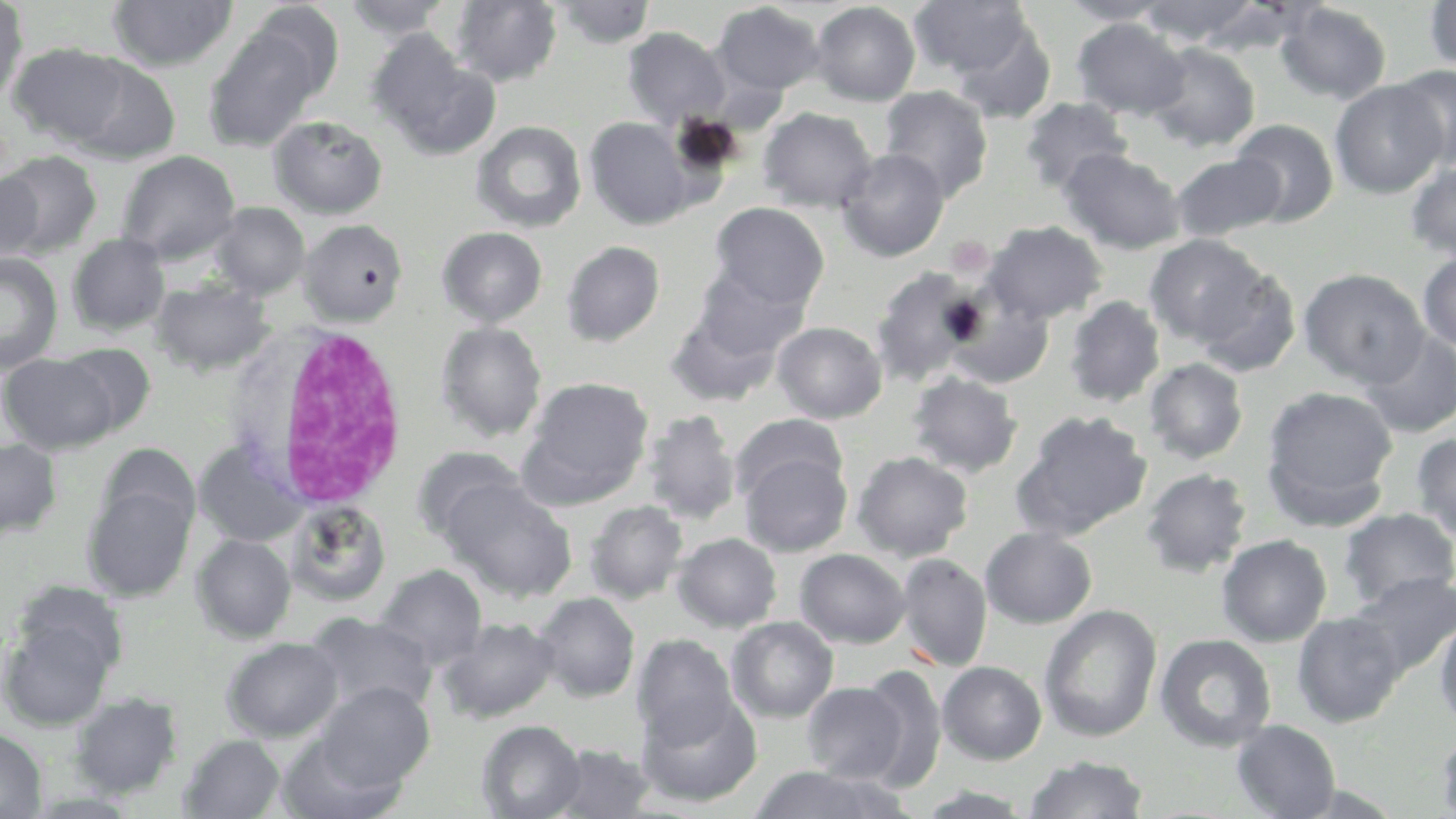

{
  "slide_level_diagnosis": "negative for blood parasites",
  "uninfected_red_blood_cell_locations": "approximate bounding boxes as named x1/y1/x2/y2 corners in pixels: (x1=450, y1=0, x2=562, y2=87), (x1=910, y1=0, x2=1032, y2=78), (x1=1137, y1=0, x2=1262, y2=46), (x1=1424, y1=0, x2=1456, y2=76), (x1=0, y1=1, x2=28, y2=106), (x1=108, y1=1, x2=238, y2=73), (x1=343, y1=1, x2=453, y2=41), (x1=551, y1=1, x2=656, y2=48), (x1=1059, y1=1, x2=1173, y2=25), (x1=245, y1=2, x2=345, y2=100), (x1=711, y1=2, x2=825, y2=98), (x1=810, y1=2, x2=921, y2=105), (x1=1276, y1=2, x2=1392, y2=104), (x1=1072, y1=18, x2=1190, y2=119), (x1=951, y1=23, x2=1057, y2=123), (x1=203, y1=27, x2=321, y2=152), (x1=623, y1=27, x2=729, y2=129), (x1=368, y1=34, x2=498, y2=158), (x1=1145, y1=42, x2=1261, y2=151), (x1=9, y1=43, x2=129, y2=146), (x1=65, y1=55, x2=181, y2=164), (x1=1390, y1=64, x2=1456, y2=169), (x1=1330, y1=80, x2=1447, y2=198), (x1=878, y1=85, x2=994, y2=202), (x1=1020, y1=97, x2=1133, y2=196), (x1=758, y1=107, x2=877, y2=213), (x1=268, y1=116, x2=388, y2=218), (x1=586, y1=118, x2=694, y2=229), (x1=1230, y1=119, x2=1339, y2=228), (x1=472, y1=120, x2=587, y2=233), (x1=837, y1=148, x2=949, y2=262), (x1=1060, y1=149, x2=1185, y2=254), (x1=0, y1=150, x2=103, y2=258), (x1=117, y1=150, x2=240, y2=264), (x1=1171, y1=152, x2=1286, y2=242), (x1=1405, y1=160, x2=1456, y2=262), (x1=1, y1=168, x2=44, y2=265), (x1=209, y1=202, x2=310, y2=300), (x1=710, y1=202, x2=829, y2=309), (x1=299, y1=219, x2=408, y2=325), (x1=983, y1=221, x2=1107, y2=325), (x1=437, y1=226, x2=548, y2=328), (x1=68, y1=233, x2=170, y2=336), (x1=1144, y1=235, x2=1269, y2=348), (x1=561, y1=240, x2=665, y2=346), (x1=1417, y1=251, x2=1456, y2=351), (x1=0, y1=253, x2=62, y2=375), (x1=689, y1=265, x2=810, y2=363), (x1=871, y1=267, x2=984, y2=386), (x1=1193, y1=267, x2=1302, y2=378), (x1=1299, y1=268, x2=1429, y2=387), (x1=151, y1=280, x2=273, y2=376), (x1=1064, y1=295, x2=1166, y2=407), (x1=947, y1=296, x2=1055, y2=388), (x1=666, y1=304, x2=784, y2=407), (x1=436, y1=322, x2=546, y2=441), (x1=773, y1=322, x2=887, y2=423), (x1=1359, y1=329, x2=1456, y2=437), (x1=56, y1=343, x2=155, y2=436), (x1=1, y1=352, x2=118, y2=454), (x1=1144, y1=358, x2=1248, y2=464), (x1=907, y1=371, x2=1022, y2=478), (x1=521, y1=377, x2=653, y2=504), (x1=1262, y1=385, x2=1398, y2=520), (x1=642, y1=410, x2=742, y2=526), (x1=1013, y1=411, x2=1153, y2=542), (x1=730, y1=413, x2=847, y2=505), (x1=1411, y1=432, x2=1456, y2=543), (x1=0, y1=438, x2=61, y2=537), (x1=194, y1=440, x2=309, y2=548), (x1=412, y1=446, x2=526, y2=545), (x1=740, y1=451, x2=852, y2=557), (x1=852, y1=451, x2=974, y2=561), (x1=1140, y1=468, x2=1252, y2=578), (x1=443, y1=478, x2=576, y2=602), (x1=83, y1=481, x2=196, y2=602), (x1=586, y1=501, x2=688, y2=604), (x1=285, y1=502, x2=392, y2=607), (x1=1339, y1=508, x2=1456, y2=609), (x1=980, y1=527, x2=1097, y2=628), (x1=673, y1=533, x2=782, y2=632), (x1=191, y1=534, x2=296, y2=643), (x1=1216, y1=535, x2=1332, y2=647), (x1=795, y1=548, x2=910, y2=648), (x1=896, y1=553, x2=992, y2=672), (x1=376, y1=565, x2=487, y2=670), (x1=1349, y1=571, x2=1456, y2=677), (x1=534, y1=592, x2=640, y2=702), (x1=1039, y1=605, x2=1162, y2=742), (x1=1291, y1=611, x2=1407, y2=727), (x1=306, y1=613, x2=437, y2=717), (x1=1, y1=615, x2=116, y2=730), (x1=1434, y1=616, x2=1456, y2=733), (x1=438, y1=617, x2=560, y2=724), (x1=727, y1=617, x2=838, y2=723), (x1=1155, y1=633, x2=1276, y2=752), (x1=633, y1=635, x2=738, y2=746), (x1=221, y1=637, x2=343, y2=742), (x1=937, y1=661, x2=1047, y2=764), (x1=859, y1=667, x2=947, y2=790), (x1=315, y1=681, x2=435, y2=790), (x1=802, y1=681, x2=910, y2=783), (x1=70, y1=692, x2=183, y2=798), (x1=637, y1=692, x2=762, y2=807), (x1=477, y1=720, x2=585, y2=818), (x1=1231, y1=720, x2=1340, y2=818), (x1=1433, y1=727, x2=1456, y2=817), (x1=0, y1=729, x2=47, y2=818), (x1=276, y1=732, x2=405, y2=819), (x1=180, y1=734, x2=286, y2=818), (x1=550, y1=743, x2=655, y2=818), (x1=1024, y1=755, x2=1148, y2=818), (x1=748, y1=765, x2=913, y2=819), (x1=912, y1=785, x2=1039, y2=817)",
  "image_size": "1456×819 pixels",
  "stain": "May-Grünwald-Giemsa",
  "magnification": "1000x",
  "preparation": "thin blood smear",
  "white_blood_cell_locations": "approximate bounding boxes as named x1/y1/x2/y2 corners in pixels: (x1=246, y1=321, x2=417, y2=514)",
  "field_of_view": "single",
  "modality": "light microscopy",
  "platelet_locations": "approximate bounding boxes as named x1/y1/x2/y2 corners in pixels: (x1=946, y1=236, x2=995, y2=279)"
}